Outline each uninfected red blood cell.
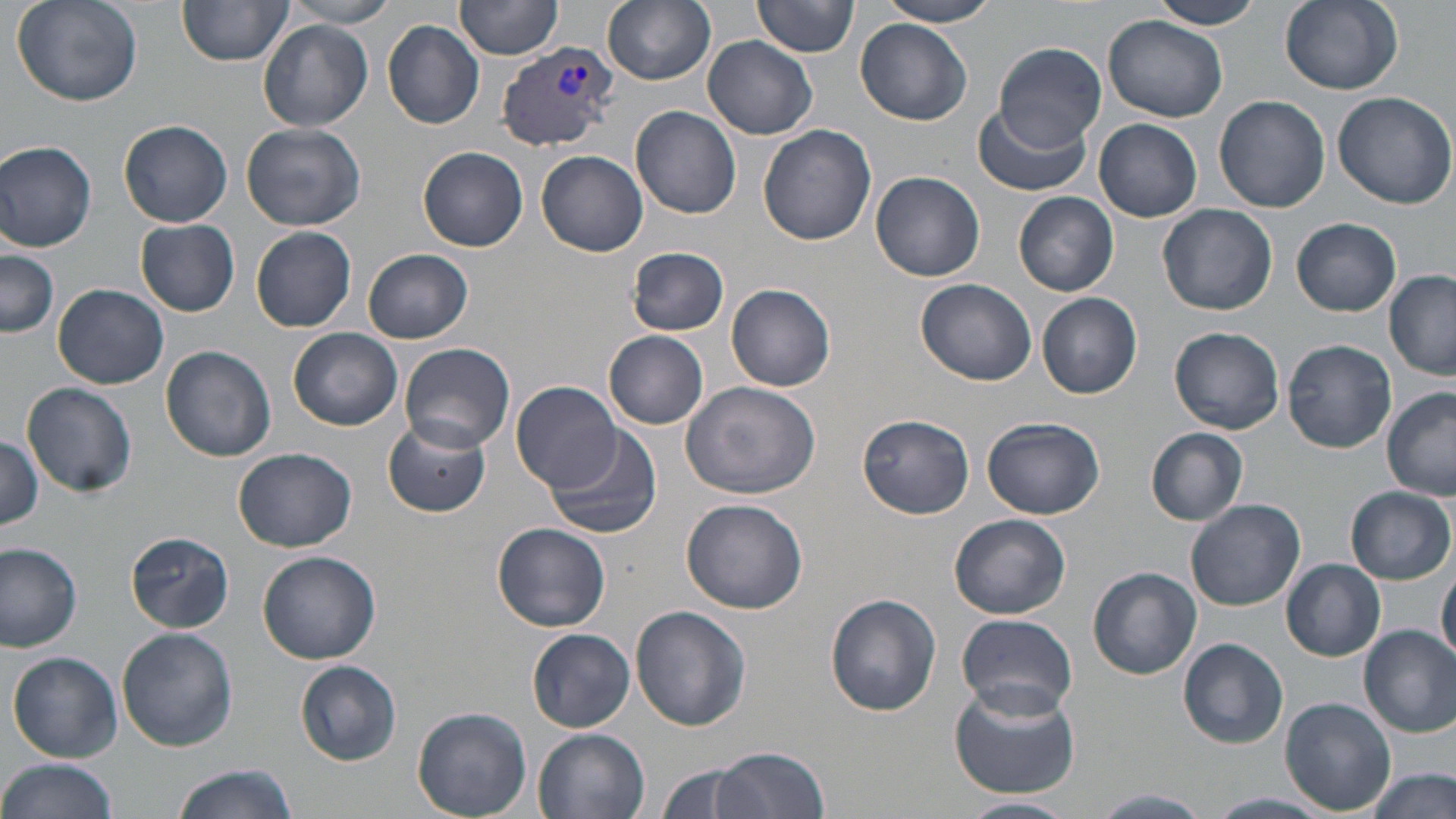
Approximate bounding boxes as named x1/y1/x2/y2 corners in pixels.
Uninfected red blood cells: (x1=10, y1=0, x2=143, y2=107), (x1=282, y1=0, x2=399, y2=29), (x1=456, y1=0, x2=564, y2=61), (x1=603, y1=0, x2=716, y2=87), (x1=754, y1=0, x2=859, y2=58), (x1=876, y1=0, x2=1005, y2=25), (x1=1148, y1=0, x2=1267, y2=30), (x1=1279, y1=0, x2=1404, y2=94), (x1=178, y1=1, x2=292, y2=68), (x1=1103, y1=15, x2=1229, y2=123), (x1=856, y1=19, x2=972, y2=125), (x1=259, y1=21, x2=373, y2=131), (x1=382, y1=21, x2=484, y2=128), (x1=704, y1=35, x2=817, y2=139), (x1=995, y1=43, x2=1105, y2=154), (x1=1329, y1=89, x2=1456, y2=209), (x1=1213, y1=95, x2=1331, y2=212), (x1=632, y1=105, x2=741, y2=219), (x1=971, y1=105, x2=1090, y2=196), (x1=1095, y1=119, x2=1201, y2=222), (x1=119, y1=120, x2=232, y2=228), (x1=240, y1=123, x2=367, y2=232), (x1=757, y1=124, x2=875, y2=247), (x1=0, y1=141, x2=98, y2=252), (x1=417, y1=146, x2=529, y2=252), (x1=536, y1=150, x2=647, y2=255), (x1=871, y1=172, x2=985, y2=282), (x1=1013, y1=192, x2=1119, y2=295), (x1=1158, y1=204, x2=1278, y2=315), (x1=135, y1=219, x2=240, y2=317), (x1=1292, y1=219, x2=1402, y2=316), (x1=251, y1=226, x2=357, y2=333), (x1=626, y1=247, x2=730, y2=337), (x1=2, y1=248, x2=61, y2=339), (x1=363, y1=249, x2=474, y2=344), (x1=1384, y1=272, x2=1456, y2=378), (x1=916, y1=277, x2=1038, y2=385), (x1=53, y1=283, x2=170, y2=388), (x1=727, y1=284, x2=836, y2=391), (x1=1038, y1=292, x2=1142, y2=399), (x1=287, y1=326, x2=403, y2=431), (x1=1170, y1=326, x2=1285, y2=434), (x1=604, y1=332, x2=710, y2=429), (x1=1283, y1=339, x2=1396, y2=453), (x1=398, y1=342, x2=516, y2=454), (x1=160, y1=345, x2=277, y2=462), (x1=681, y1=379, x2=823, y2=498), (x1=512, y1=381, x2=624, y2=493), (x1=22, y1=382, x2=137, y2=498), (x1=1382, y1=387, x2=1456, y2=501), (x1=857, y1=413, x2=974, y2=520), (x1=383, y1=416, x2=490, y2=518), (x1=983, y1=417, x2=1108, y2=521), (x1=546, y1=425, x2=661, y2=541), (x1=1146, y1=428, x2=1247, y2=524), (x1=0, y1=435, x2=44, y2=532), (x1=233, y1=448, x2=357, y2=552), (x1=1346, y1=487, x2=1454, y2=584), (x1=681, y1=498, x2=807, y2=613), (x1=1186, y1=499, x2=1306, y2=612), (x1=949, y1=514, x2=1071, y2=617), (x1=493, y1=522, x2=611, y2=633), (x1=126, y1=531, x2=233, y2=632), (x1=0, y1=544, x2=82, y2=650), (x1=257, y1=548, x2=381, y2=664), (x1=1281, y1=559, x2=1386, y2=660), (x1=1436, y1=561, x2=1456, y2=666), (x1=1088, y1=566, x2=1201, y2=680), (x1=825, y1=593, x2=942, y2=714), (x1=631, y1=605, x2=751, y2=732), (x1=956, y1=613, x2=1080, y2=716), (x1=1359, y1=626, x2=1456, y2=737), (x1=116, y1=627, x2=238, y2=752), (x1=529, y1=629, x2=634, y2=731), (x1=1179, y1=637, x2=1288, y2=749), (x1=9, y1=652, x2=122, y2=761), (x1=296, y1=661, x2=400, y2=764), (x1=948, y1=679, x2=1081, y2=799), (x1=1282, y1=697, x2=1395, y2=815), (x1=413, y1=706, x2=532, y2=819), (x1=531, y1=726, x2=653, y2=819), (x1=712, y1=747, x2=830, y2=819), (x1=0, y1=758, x2=119, y2=819), (x1=651, y1=762, x2=770, y2=819), (x1=172, y1=765, x2=296, y2=819), (x1=1367, y1=768, x2=1453, y2=818), (x1=1095, y1=790, x2=1212, y2=817), (x1=1207, y1=792, x2=1334, y2=818), (x1=954, y1=797, x2=1077, y2=818).

{
  "slide_level_diagnosis": "Plasmodium vivax",
  "image_size": "1456×819 pixels",
  "plasmodium_vivax_infected_red_blood_cell_locations": "approximate bounding boxes as named x1/y1/x2/y2 corners in pixels: (x1=494, y1=40, x2=613, y2=151)",
  "preparation": "thin blood film",
  "field_of_view": "one of a larger specimen",
  "modality": "optical microscopy",
  "magnification": "1000x",
  "stain": "May-Grünwald-Giemsa"
}